Comment on the morphology of the erythrocytes.
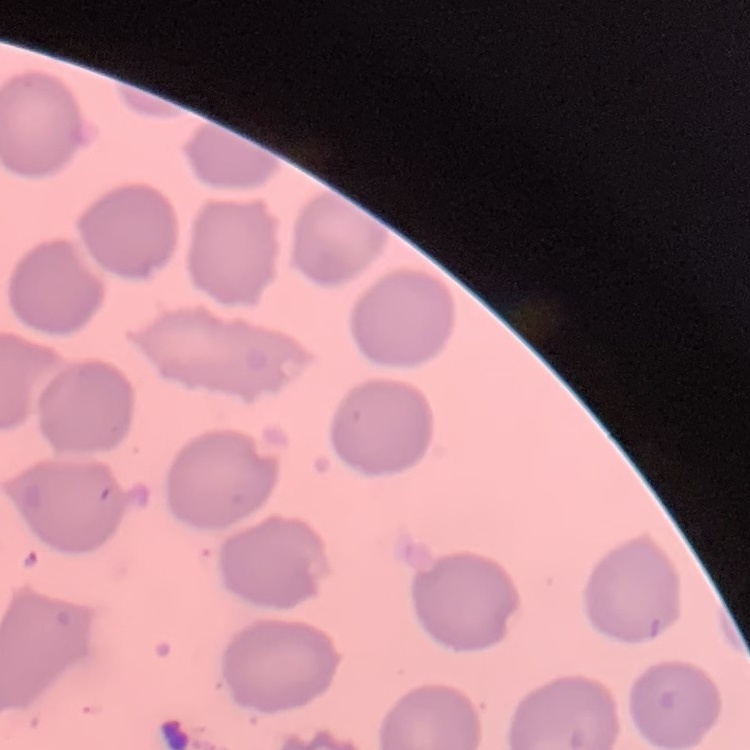

No rouleaux formation.

Summary:
  - Image type: square crop of a larger photomicrograph
  - Stain: Field's or Giemsa
  - Preparation: thin blood smear